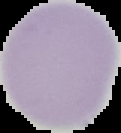
Summary:
  - Image type: segmented cell region with the area outside set to black
  - Result: no Plasmodium parasites detected
  - Preparation: thin blood film
  - Image size: 121×133 pixels